Describe the morphology of the erythrocytes.
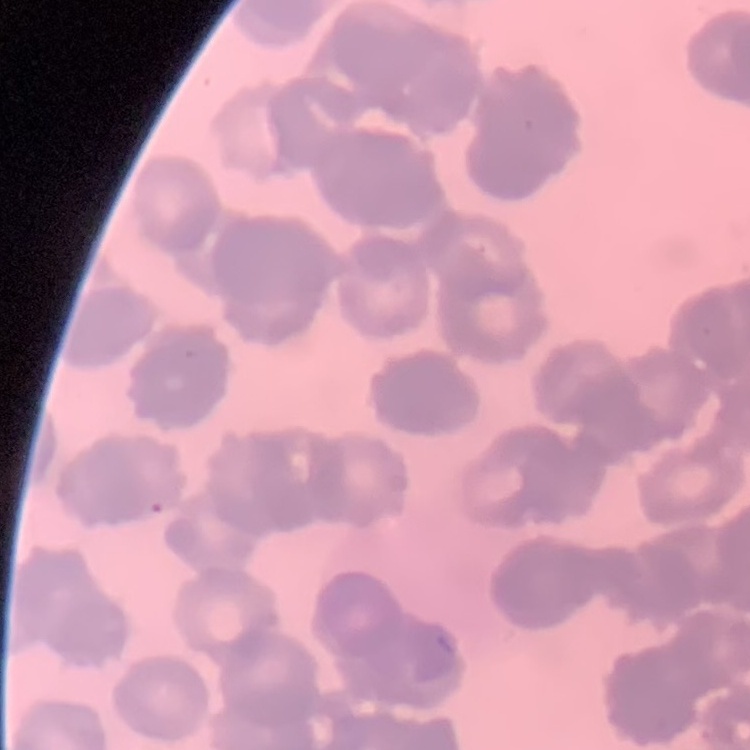

Rouleaux formation.

Field's or Giemsa stain. Square crop of a larger photomicrograph. Thin blood film.